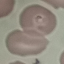

Malaria status: parasitized. Thin blood film. Photographed with a smartphone camera at the microscope eyepiece. Automatically extracted cell patch, resized to 64 × 64 pixels. Giemsa stain.